Comment on the morphology of the erythrocytes.
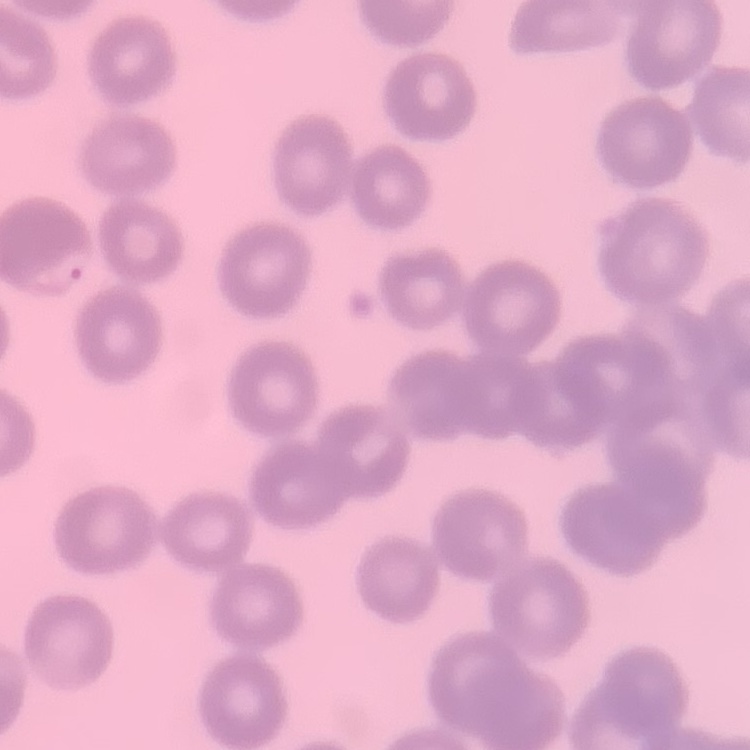
No rouleaux formation.

Summary:
  - Stain: Field's or Giemsa
  - Preparation: thin peripheral smear
  - Image type: one tile cut from a larger photomicrograph